Assess the morphology of the erythrocytes.
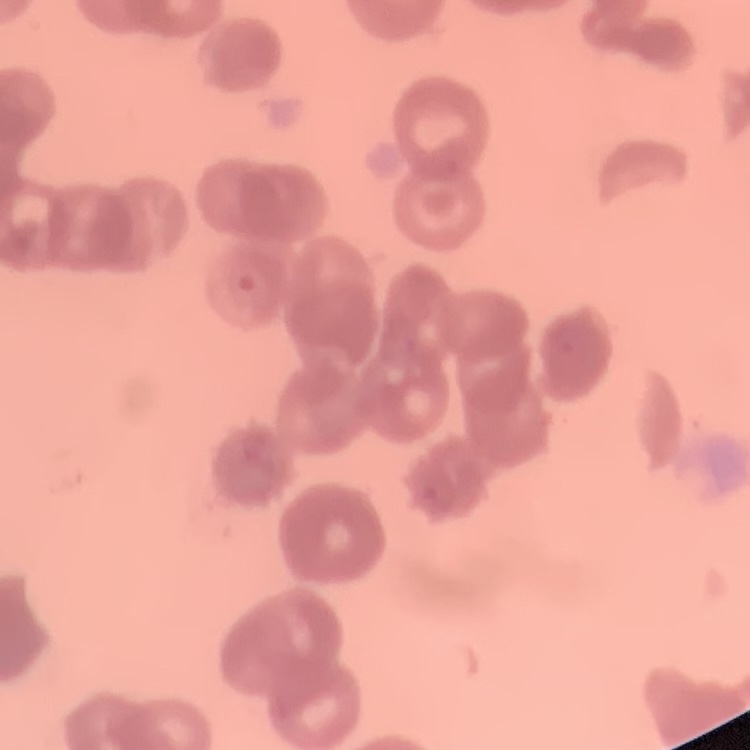
They show rouleaux formation.

image_type: one tile cut from a larger photomicrograph
stain: Field's or Giemsa
preparation: thin peripheral smear